Outline each uninfected red blood cell.
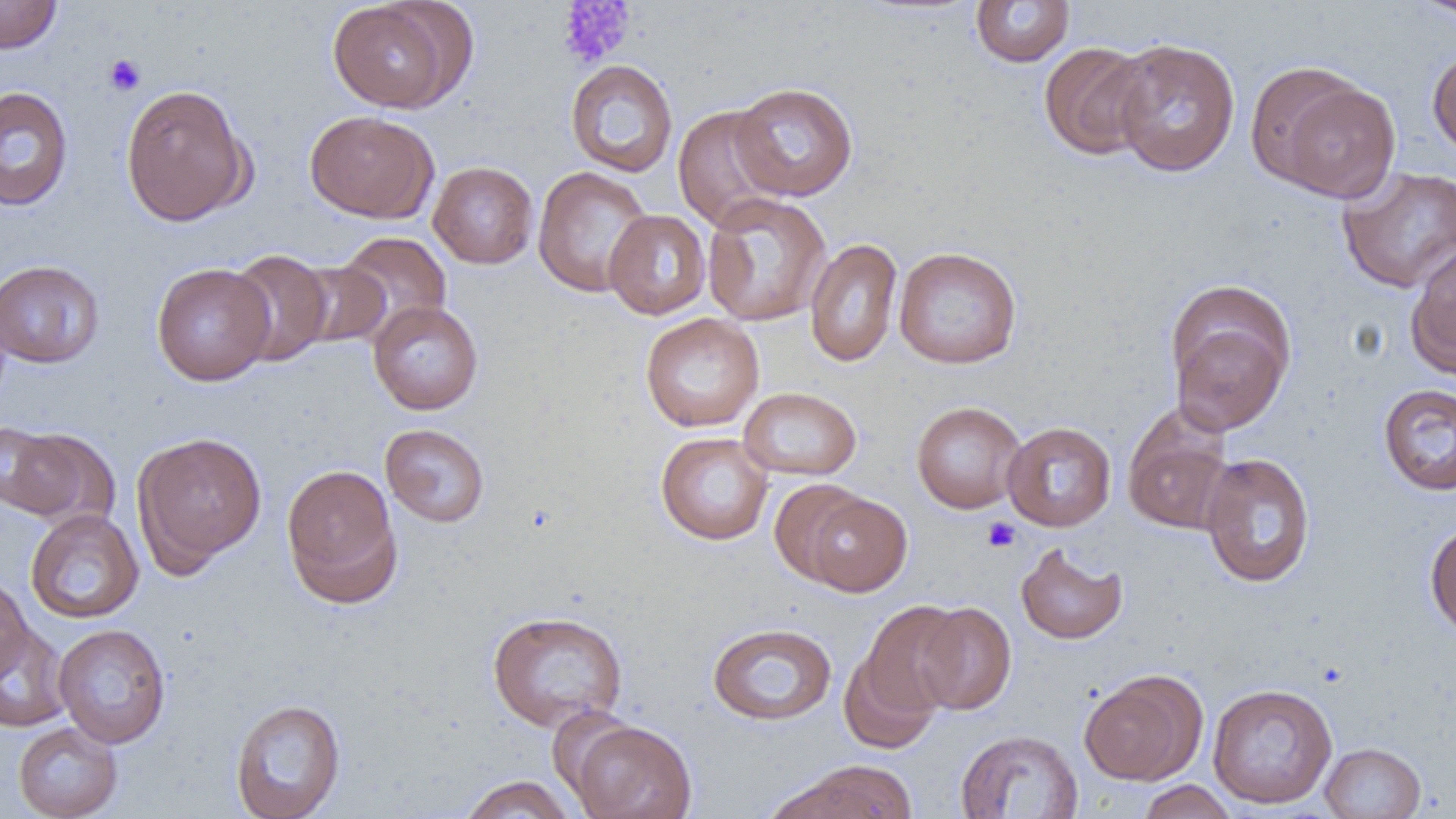

Approximate bounding boxes as [x1, y1, x2, y2] in pixels.
Uninfected red blood cells: [0, 0, 62, 54], [327, 0, 462, 113], [1409, 0, 1456, 21], [970, 1, 1075, 67], [1109, 38, 1241, 177], [1038, 41, 1154, 160], [1427, 46, 1456, 159], [565, 59, 678, 177], [1271, 76, 1401, 203], [731, 82, 858, 201], [120, 83, 252, 226], [0, 85, 74, 211], [671, 104, 790, 232], [304, 109, 439, 223], [428, 161, 539, 269], [1336, 165, 1456, 294], [533, 166, 654, 298], [702, 192, 831, 327], [604, 209, 711, 320], [337, 231, 452, 339], [805, 238, 903, 368], [1406, 240, 1456, 377], [893, 246, 1022, 369], [226, 249, 334, 367], [0, 260, 104, 368], [290, 261, 391, 350], [151, 263, 275, 386], [1166, 282, 1297, 435], [369, 300, 483, 415], [640, 313, 764, 432], [1378, 383, 1456, 496], [738, 387, 862, 481], [911, 400, 1027, 514], [1122, 409, 1235, 535], [1002, 421, 1116, 531], [381, 424, 490, 527], [1, 428, 110, 526], [133, 431, 267, 570], [655, 432, 774, 546], [1199, 452, 1316, 588], [281, 463, 402, 605], [768, 478, 870, 586], [802, 491, 912, 597], [25, 508, 144, 624], [1424, 518, 1456, 637], [1016, 542, 1127, 644], [0, 573, 32, 685], [859, 600, 967, 718], [914, 602, 1016, 715], [486, 610, 628, 732], [707, 622, 837, 726], [53, 623, 171, 748], [0, 624, 72, 733], [838, 647, 941, 755], [1079, 670, 1206, 785], [1207, 683, 1338, 809], [229, 698, 346, 818], [567, 719, 697, 819], [12, 722, 123, 819], [955, 729, 1084, 818], [1320, 742, 1426, 819], [769, 761, 918, 818], [458, 774, 577, 819], [1136, 780, 1239, 819].

slide-level diagnosis = negative for blood parasites
field of view = single
platelet locations = approximate bounding boxes as [x1, y1, x2, y2] in pixels: [556, 1, 634, 69], [104, 54, 146, 96], [982, 517, 1020, 552]
preparation = thin blood film
modality = optical microscopy
image size = 1456×819 pixels
magnification = 1000x